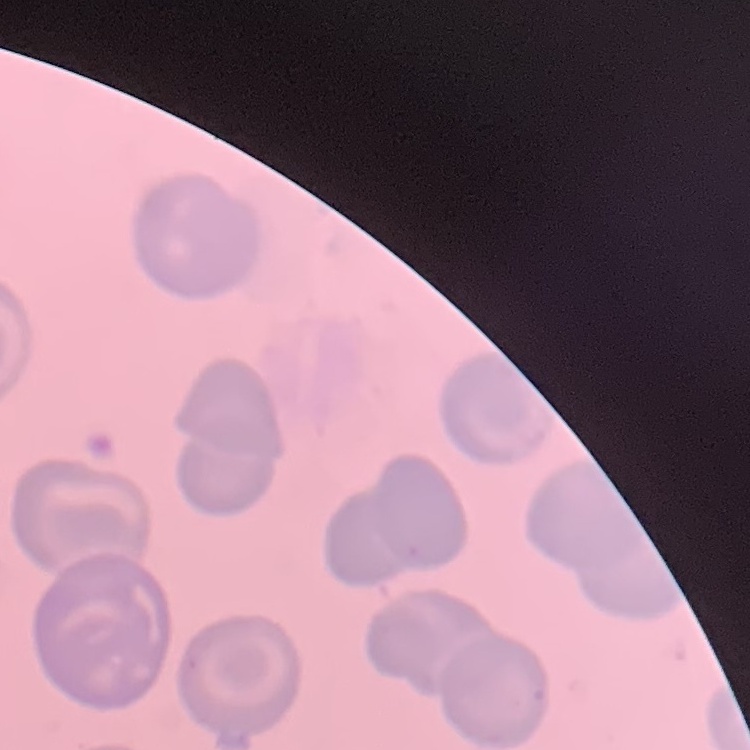 The red blood cells show no rouleaux formation. Stained with either Field's or Giemsa. Thin blood film. One tile cut from a larger photomicrograph.